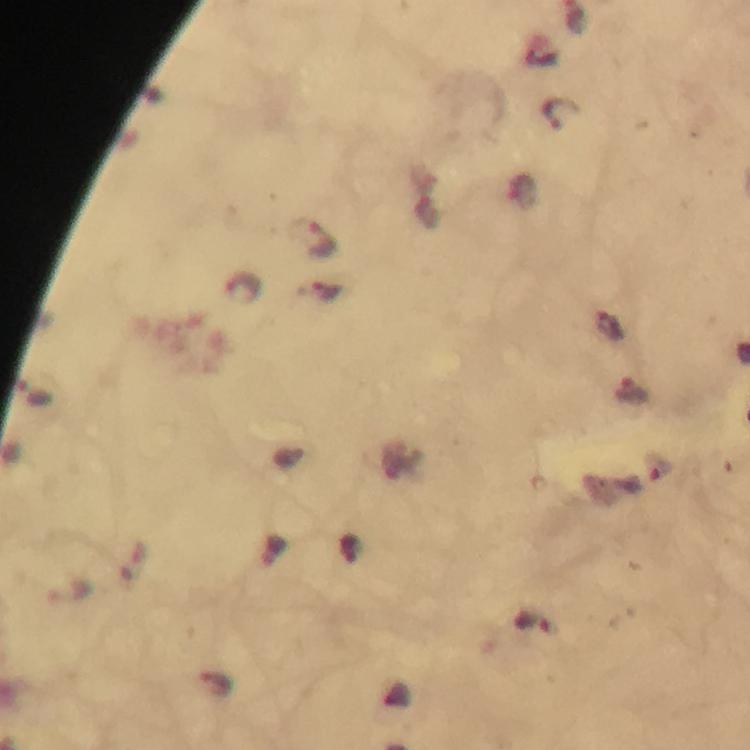

Approximate centers as {x, y} in pixels. Plasmodium parasite locations: {561, 111}, {314, 238}, {240, 287}, {319, 291}, {610, 324}, {633, 391}, {533, 624}, {217, 686}. At 100x magnification. Thick blood smear. Giemsa stain. From a malaria diagnostic workup. Image is 750×750 pixels. A crop from one field of view. Immersion oil was used. Photographed with a smartphone mounted on the microscope.